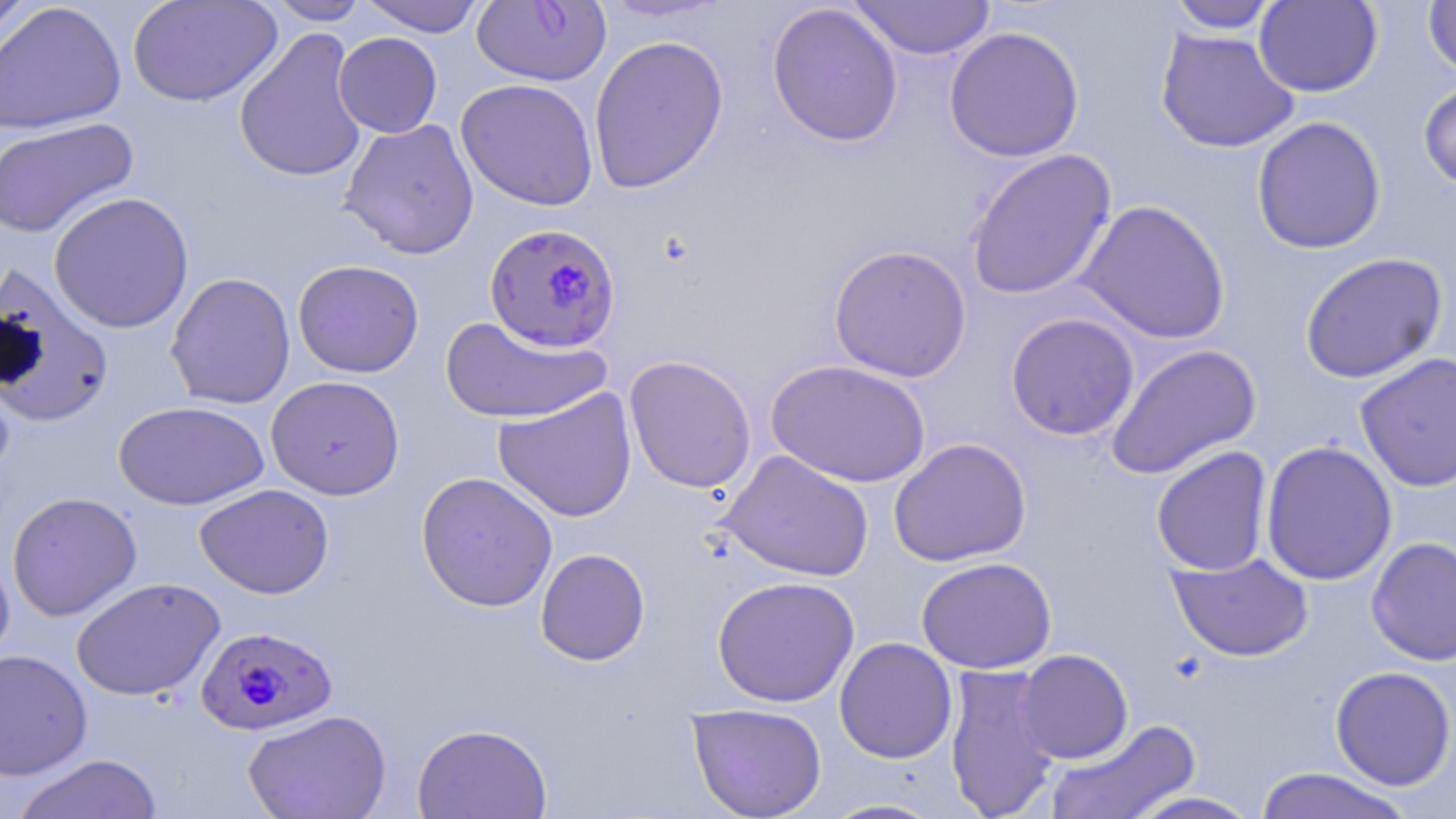
{
  "slide_level_diagnosis": "Plasmodium falciparum",
  "modality": "light microscopy",
  "image_size": "1456×819 pixels",
  "stain": "May-Grünwald-Giemsa",
  "field_of_view": "single",
  "uninfected_red_blood_cell_locations": "approximate bounding boxes as (x1, y1, x2, y2) in pixels: (1, 0, 35, 59), (127, 0, 282, 108), (263, 0, 372, 25), (356, 0, 488, 37), (596, 0, 732, 23), (847, 0, 996, 60), (1254, 0, 1383, 97), (1422, 0, 1456, 81), (0, 1, 126, 135), (1165, 1, 1283, 33), (766, 3, 904, 148), (944, 26, 1084, 163), (234, 27, 369, 184), (1155, 29, 1300, 153), (333, 32, 442, 138), (588, 35, 729, 193), (456, 78, 599, 211), (1417, 79, 1456, 192), (1251, 116, 1386, 254), (0, 118, 139, 239), (339, 119, 479, 259), (964, 148, 1118, 301), (48, 191, 195, 334), (1075, 199, 1231, 344), (828, 244, 972, 382), (1299, 252, 1448, 384), (285, 259, 414, 500), (292, 259, 424, 378), (0, 262, 114, 428), (165, 272, 296, 409), (1005, 313, 1140, 441), (440, 315, 611, 424), (1105, 343, 1262, 480), (1355, 352, 1456, 492), (623, 355, 757, 494), (766, 359, 931, 487), (266, 375, 405, 500), (493, 387, 637, 522), (113, 401, 270, 510), (888, 437, 1031, 567), (1260, 440, 1397, 586), (1151, 446, 1273, 576), (719, 449, 874, 582), (416, 471, 558, 612), (195, 483, 334, 599), (7, 491, 142, 621), (1366, 537, 1456, 666), (0, 544, 15, 669), (535, 548, 651, 666), (1167, 552, 1314, 662), (916, 556, 1056, 674), (711, 575, 860, 707), (71, 576, 226, 701), (834, 637, 958, 763), (0, 649, 92, 781), (1014, 649, 1133, 764), (944, 662, 1062, 819), (1330, 666, 1456, 790), (687, 703, 827, 818), (242, 708, 392, 819), (1043, 718, 1202, 819), (411, 722, 553, 818), (11, 753, 162, 819), (1253, 766, 1415, 819), (1123, 790, 1264, 818), (819, 798, 948, 818)",
  "magnification": "1000x",
  "preparation": "thin blood smear",
  "plasmodium_falciparum_infected_red_blood_cell_locations": "approximate bounding boxes as (x1, y1, x2, y2) in pixels: (472, 0, 612, 87), (484, 224, 623, 353), (196, 625, 338, 735)"
}